Assess this cell for malaria.
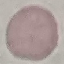

Uninfected.

Giemsa stain. Photographed with a smartphone camera at the microscope eyepiece. Cell patch, automatically extracted from a larger field of view and resized to 64 × 64 pixels. Thin blood smear.